Classify this cell by malaria status.
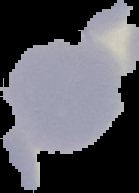

It is uninfected.

Summary:
  - Preparation: thin blood smear
  - Image size: 139×193 pixels
  - Image type: cell region segmented out of the field of view; surrounding area masked to black